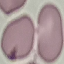

Summary:
  - Malaria status: uninfected
  - Image type: automatically extracted cell patch, resized to 64 × 64 pixels
  - Capture: smartphone through the microscope eyepiece
  - Stain: Giemsa
  - Preparation: thin blood smear